Classify this cell by malaria status.
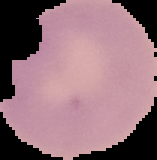
It is uninfected.

From a thin blood film. Cell region segmented out of the field of view; the surrounding area is masked to black. Image is 157×160 pixels.